Report the malaria status of this cell.
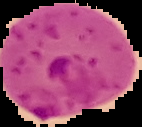

It is parasitized.

Summary:
  - Image type: segmented cell region with the area outside set to black
  - Image size: 142×127 pixels
  - Preparation: thin blood smear